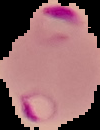

Result: malaria parasites detected. From a thin blood smear. Image is 100×130 pixels. The area outside the segmented cell region is set to black.